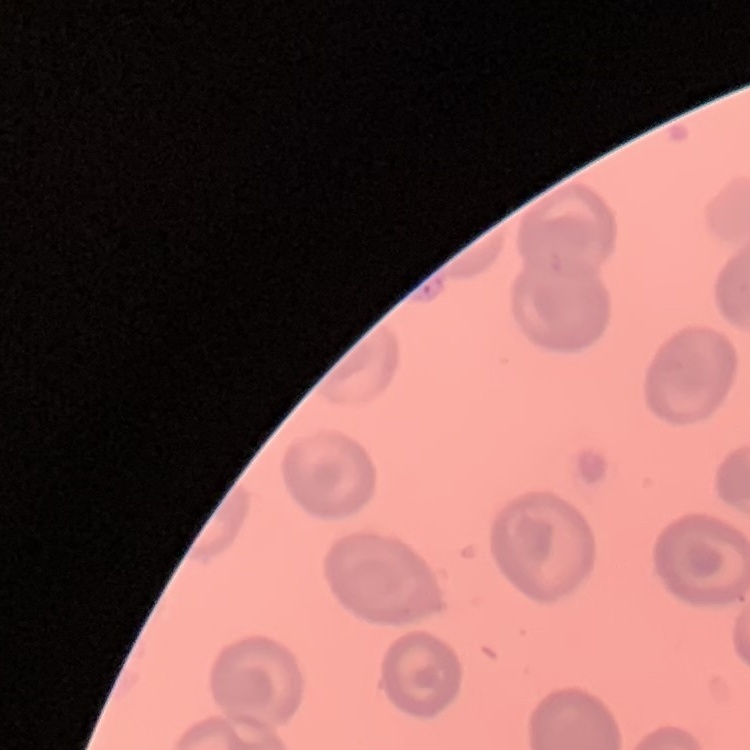
red blood cell morphology = no rouleaux formation
stain = Field's or Giemsa
preparation = thin blood film
image type = square crop of a larger photomicrograph